Give the preparation type.
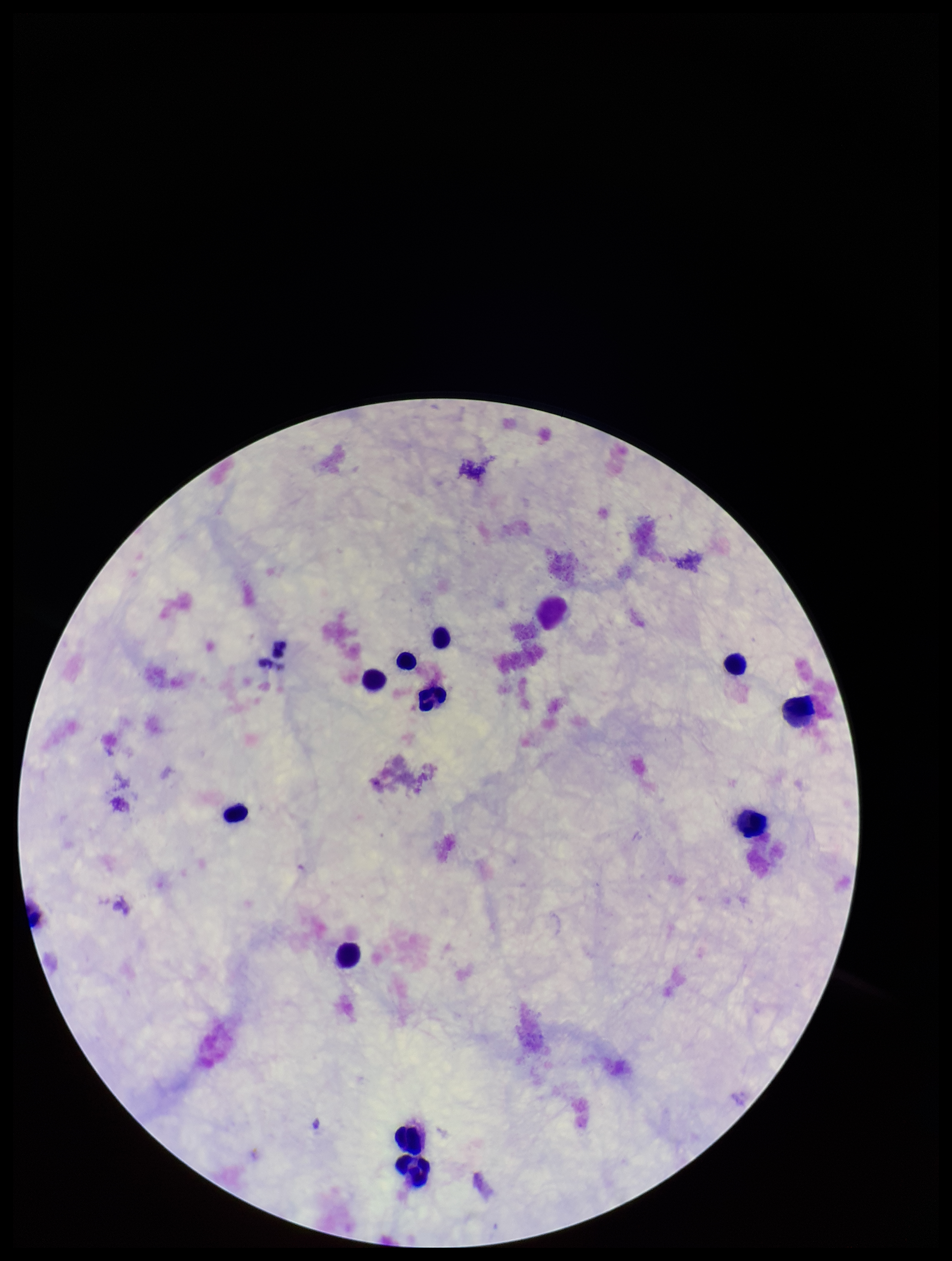

Thick.

Plasmodium parasites = none detected
capture = smartphone photograph through the microscope eyepiece
stain = Giemsa
patient malaria status = negative
leukocyte count = 11
field of view = one from this slide
image size = 952×1261 pixels
parasite count = 0